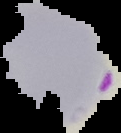 From a thin blood film. Result: malaria parasites identified. Segmented cell region on a black background. Image is 121×133 pixels.